Give the position of every Plasmodium parasite visible.
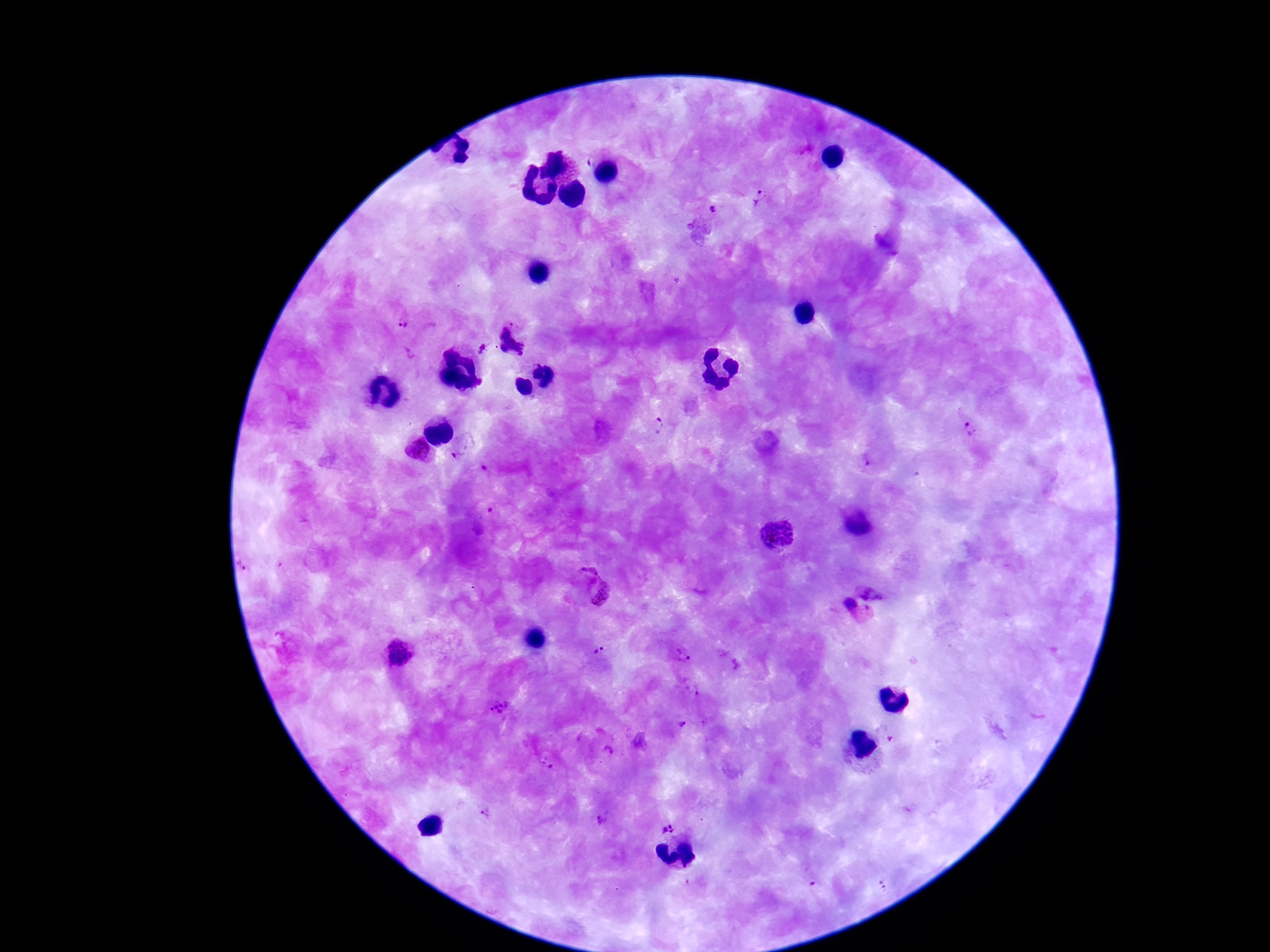

Approximate object centers, in pixels from the top-left corner.
Plasmodium parasites: (x=760, y=200), (x=712, y=211), (x=400, y=324), (x=518, y=336), (x=484, y=347), (x=660, y=426), (x=970, y=428), (x=461, y=454), (x=868, y=463), (x=775, y=533), (x=873, y=584), (x=588, y=585), (x=842, y=612), (x=595, y=650), (x=402, y=653), (x=681, y=659), (x=691, y=688), (x=497, y=707), (x=683, y=725), (x=606, y=752), (x=547, y=763), (x=484, y=813), (x=601, y=820), (x=667, y=827).

Summary:
  - Magnification: 100x
  - Capture: smartphone camera through the microscope eyepiece
  - Field of view: one from this slide
  - Stain: Giemsa
  - Preparation: thick peripheral-blood smear
  - Patient malaria status: infected
  - Image size: 1270×952 pixels